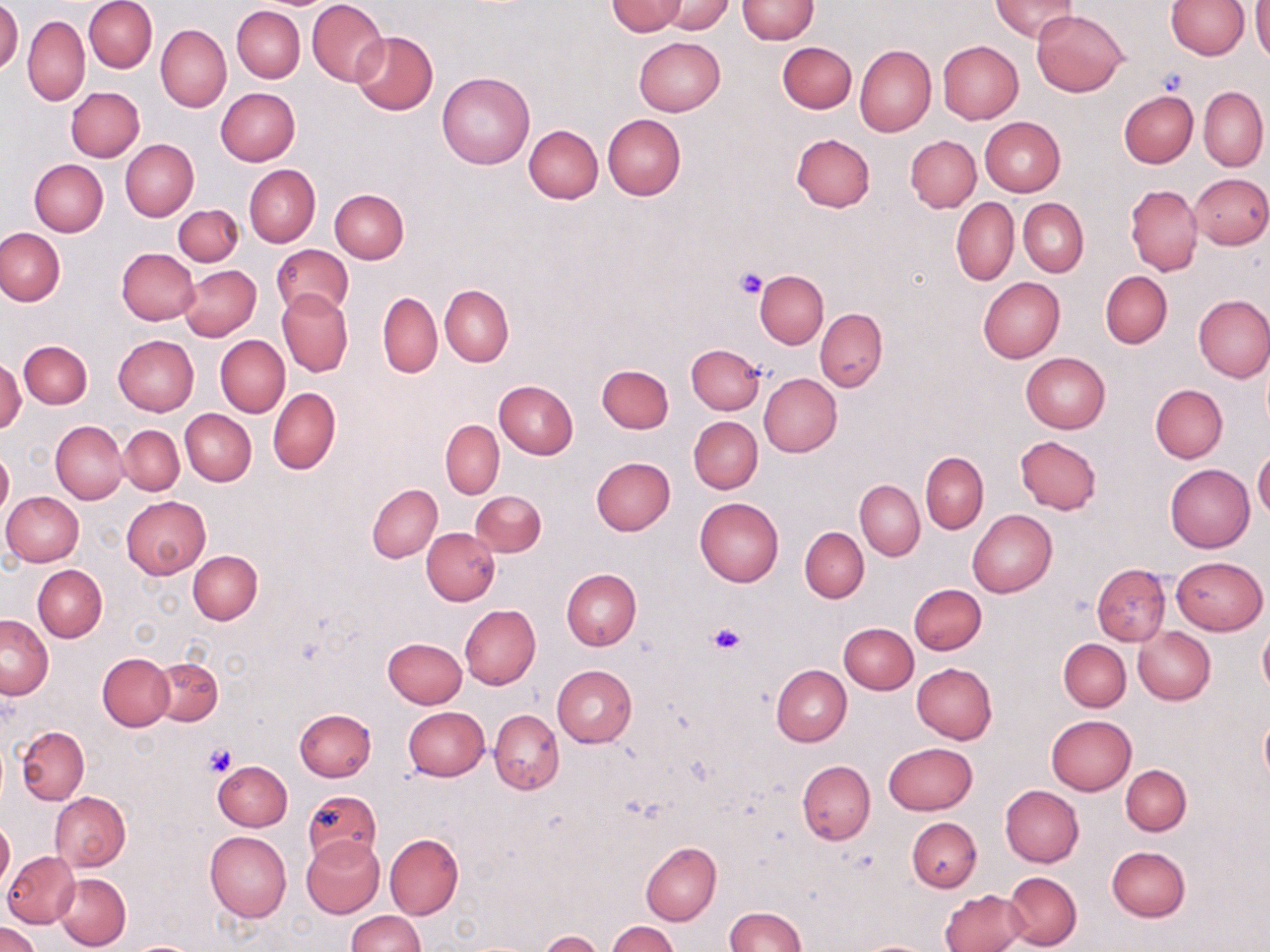
Summary:
  - Coordinate format: approximate bounding boxes as (x1,y1)-(x2,y2) corner pairs in pixels
  - Uninfected red blood cell locations: (84,0)-(157,73), (307,0)-(388,87), (738,0)-(818,44), (1165,0)-(1250,59), (607,1)-(687,35), (659,1)-(731,34), (992,1)-(1079,42), (0,2)-(22,74), (1251,3)-(1270,65), (232,6)-(304,82), (1031,9)-(1128,96), (22,15)-(90,105), (155,23)-(231,112), (350,31)-(437,115), (633,37)-(724,115), (778,42)-(856,113), (938,42)-(1023,124), (854,45)-(936,137), (436,72)-(535,169), (67,86)-(144,161), (1199,86)-(1268,172), (216,87)-(299,165), (1119,90)-(1198,167), (603,114)-(686,200), (979,116)-(1065,196), (524,124)-(603,203), (790,133)-(875,212), (905,134)-(981,213), (120,139)-(198,221), (29,158)-(108,237), (244,164)-(320,247), (1190,173)-(1270,249), (1125,183)-(1203,276), (330,189)-(409,264), (951,198)-(1019,286), (1019,198)-(1088,277), (173,204)-(242,266), (0,227)-(65,306), (272,245)-(354,320), (116,248)-(199,325), (179,265)-(261,341), (755,270)-(828,349), (1100,270)-(1172,348), (977,277)-(1064,364), (440,285)-(513,366), (277,289)-(352,376), (378,292)-(442,378), (1193,294)-(1270,382), (815,308)-(887,392), (112,335)-(198,416), (215,336)-(289,416), (19,340)-(92,408), (686,344)-(763,413), (1021,353)-(1111,433), (0,356)-(24,431), (597,365)-(673,434), (758,373)-(841,457), (494,380)-(577,459), (1150,384)-(1227,463), (267,387)-(341,475), (180,409)-(256,486), (689,417)-(762,493), (441,419)-(504,498), (51,421)-(128,504), (119,425)-(184,495), (1015,435)-(1102,514), (1,447)-(13,517), (1253,448)-(1270,522), (921,452)-(988,533), (590,458)-(675,536), (1165,465)-(1254,553), (855,479)-(924,560), (368,483)-(442,563), (470,490)-(545,557), (2,492)-(83,565), (121,495)-(210,578), (694,497)-(784,587), (968,510)-(1057,597), (799,527)-(868,603), (422,528)-(499,605), (188,550)-(263,624), (1170,556)-(1266,635), (1092,564)-(1171,645), (34,565)-(107,642), (562,569)-(641,650), (909,583)-(986,655), (460,604)-(541,689), (1,615)-(53,698), (1258,620)-(1270,697), (838,622)-(919,694), (1133,626)-(1216,703), (382,637)-(467,708), (1059,639)-(1130,711), (99,654)-(174,730), (150,658)-(224,725), (913,663)-(997,744), (551,664)-(636,747), (772,665)-(851,746), (403,706)-(488,780), (295,708)-(376,781), (1259,708)-(1270,788), (489,709)-(564,794), (1045,715)-(1136,795), (16,726)-(89,804), (883,742)-(977,815), (212,760)-(291,831), (797,760)-(876,844), (1121,765)-(1191,835), (1000,785)-(1083,868), (302,789)-(382,866), (50,791)-(131,872), (906,817)-(982,892), (1,819)-(15,894), (205,831)-(292,922), (385,833)-(464,918), (301,837)-(384,918), (640,842)-(721,925), (1106,846)-(1190,922), (3,851)-(79,927), (54,872)-(131,950), (1003,872)-(1080,948), (941,888)-(1029,952), (724,906)-(807,952), (346,911)-(423,951), (607,920)-(679,952), (0,922)-(41,952), (538,931)-(605,951), (854,939)-(940,952), (129,941)-(200,952)
  - Platelet locations: (1154,68)-(1190,99), (735,268)-(766,298), (707,622)-(747,655), (204,741)-(237,775)
  - Slide-level diagnosis: negative for blood parasites
  - Modality: light microscopy
  - Image size: 1270×952 pixels
  - Preparation: thin blood film
  - Stain: May-Grünwald-Giemsa
  - Field of view: single
  - Magnification: 1000x